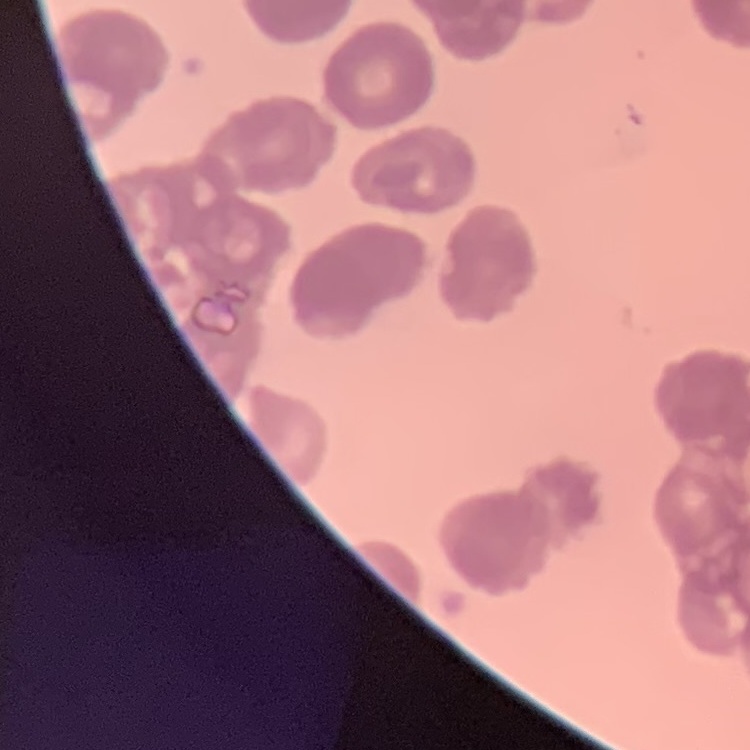
Summary:
  - Red blood cell morphology: rouleaux formation
  - Preparation: thin peripheral smear
  - Image type: square crop of a larger photomicrograph
  - Stain: Field's or Giemsa